Assess this cell for malaria.
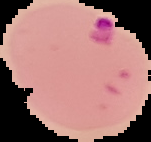

Parasitized.

image size = 151×142 pixels
preparation = thin blood film
image type = segmented cell region with the area outside set to black